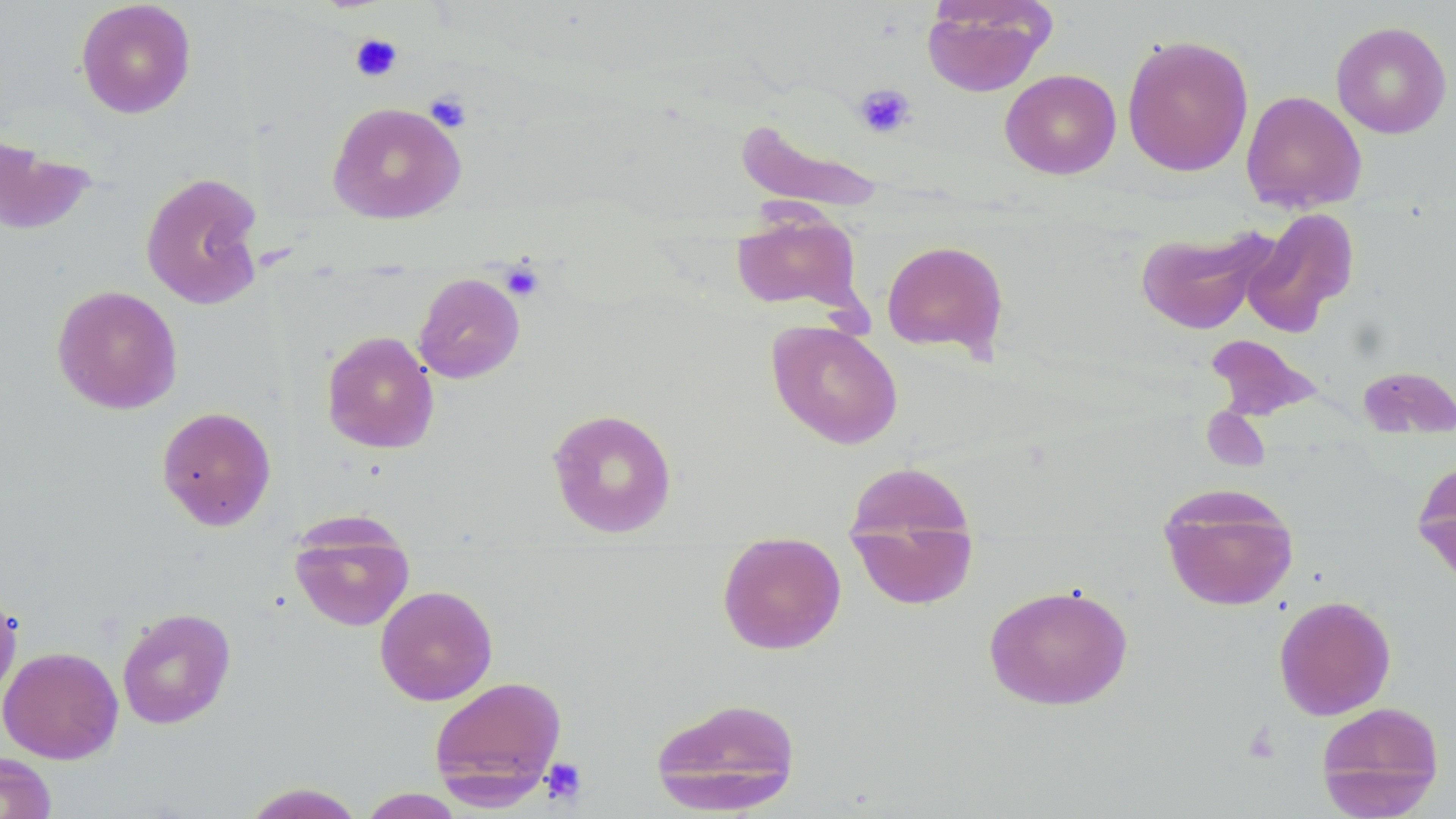

slide-level diagnosis = no evidence of blood parasites
platelet locations = approximate bounding boxes as [x1, y1, x2, y2] in pixels: [349, 33, 403, 83], [854, 83, 916, 139], [424, 91, 472, 132], [499, 260, 545, 302], [1242, 721, 1281, 765], [540, 757, 587, 805]
field of view = single
uninfected red blood cell locations = approximate bounding boxes as [x1, y1, x2, y2] in pixels: [75, 1, 197, 118], [921, 1, 1054, 96], [1330, 21, 1452, 139], [1122, 34, 1254, 176], [1000, 68, 1121, 179], [1241, 90, 1367, 213], [327, 101, 466, 224], [736, 117, 885, 213], [0, 131, 97, 236], [140, 171, 266, 310], [1242, 208, 1359, 337], [730, 209, 863, 316], [1136, 227, 1273, 334], [881, 239, 1009, 360], [413, 273, 525, 383], [52, 284, 183, 414], [767, 320, 903, 449], [321, 330, 439, 454], [1205, 334, 1324, 422], [1357, 365, 1455, 441], [156, 405, 276, 531], [546, 407, 678, 538], [1413, 458, 1456, 588], [843, 461, 981, 609], [1158, 482, 1299, 612], [289, 515, 415, 632], [717, 537, 847, 655], [983, 583, 1133, 711], [374, 585, 498, 705], [0, 591, 22, 704], [1273, 594, 1396, 720], [117, 608, 236, 729], [0, 646, 124, 764], [428, 675, 567, 802], [649, 695, 802, 815], [1315, 701, 1445, 818], [0, 752, 56, 819], [240, 783, 366, 818], [358, 788, 466, 818]
magnification = 1000x
preparation = thin blood smear
modality = light microscopy
stain = May-Grünwald-Giemsa
image size = 1456×819 pixels